State which parasite is depicted.
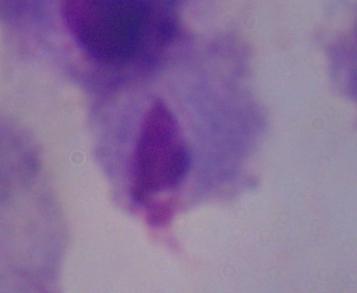
A trichomonad.

modality = photomicrograph
magnification = 1000x